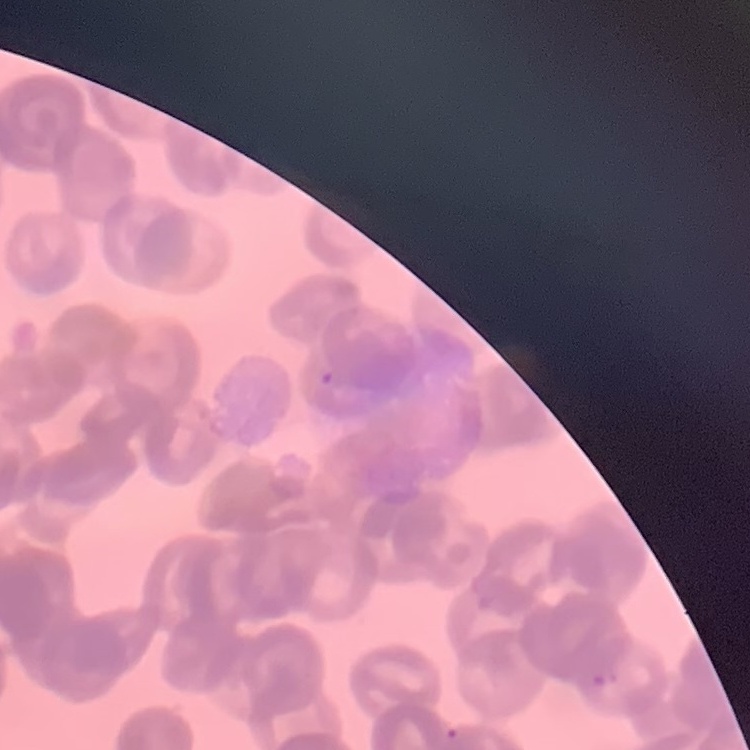
Summary:
  - Red blood cell morphology: rouleaux formation
  - Image type: square crop of a larger photomicrograph
  - Preparation: thin peripheral smear
  - Stain: Field's or Giemsa